Report the malaria status of this cell.
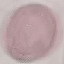
It is uninfected.

{
  "stain": "Giemsa",
  "image_type": "automatically extracted cell patch, resized to 64 × 64 pixels",
  "preparation": "thin blood smear",
  "capture": "smartphone camera at the microscope eyepiece"
}